Give the preparation type.
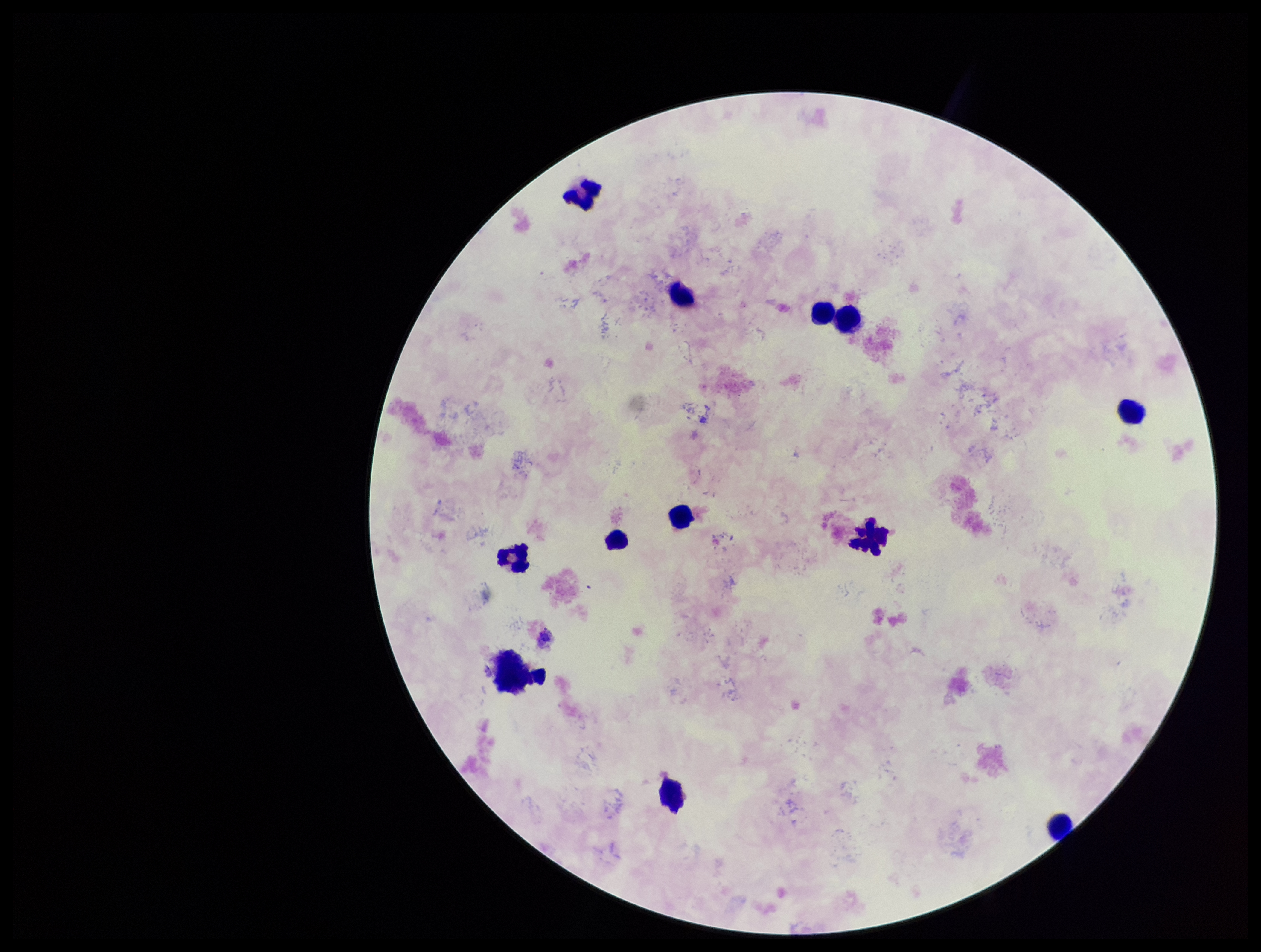

Thick.

Summary:
  - Parasite count: 0
  - Capture: smartphone photograph through the microscope eyepiece
  - Patient malaria status: infected
  - Leukocyte count: 11
  - Image size: 1261×952 pixels
  - Field of view: one from this slide
  - Species reported for this patient: Plasmodium falciparum
  - Stain: Giemsa
  - Plasmodium parasites: none identified